Comment on the morphology of the erythrocytes.
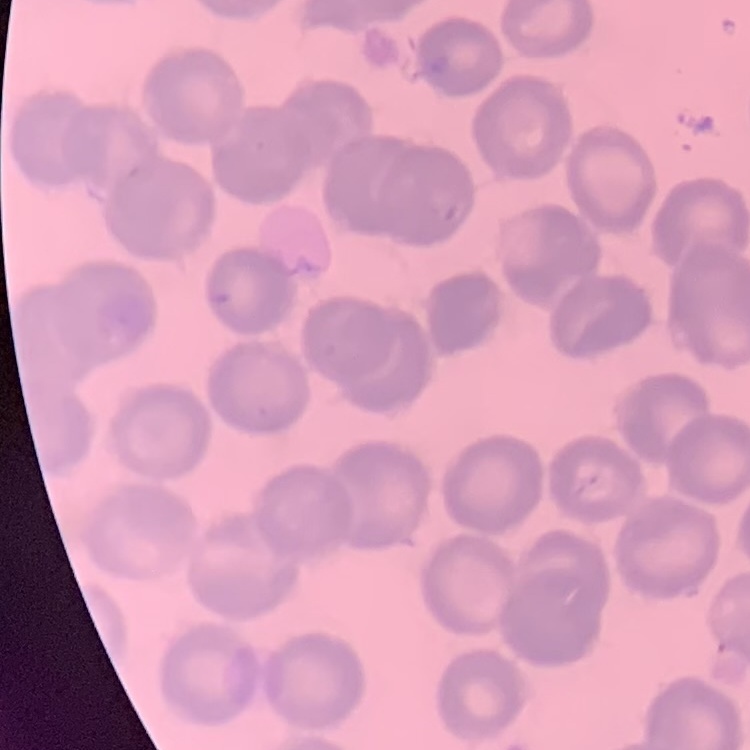

No rouleaux formation.

Square crop of a larger photomicrograph. Stained with either Field's or Giemsa. Thin peripheral smear.